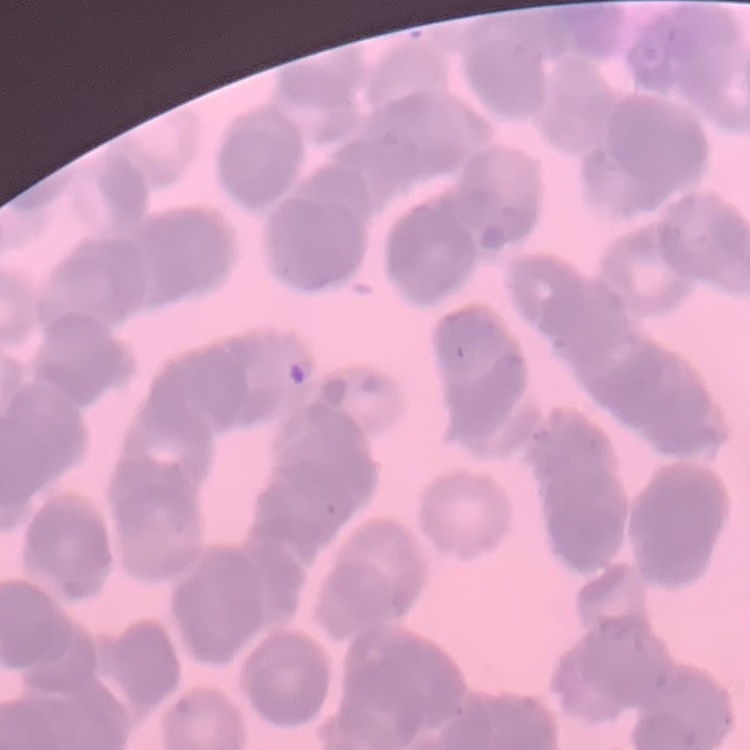
red_blood_cell_morphology: rouleaux formation
preparation: thin peripheral smear
stain: Field's or Giemsa
image_type: square crop of a larger photomicrograph